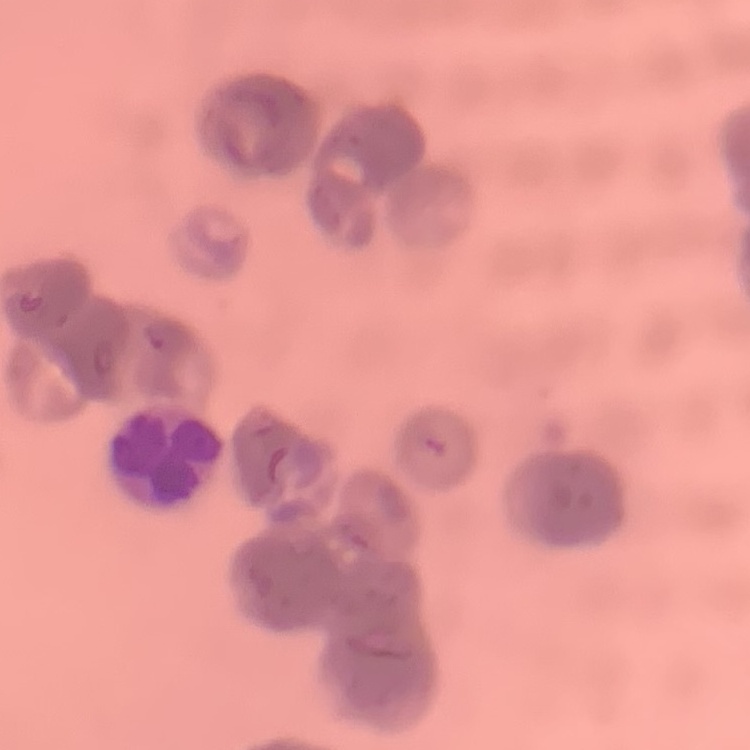
The erythrocytes show rouleaux formation. Field's or Giemsa stain. Thin blood film. One tile cut from a larger photomicrograph.